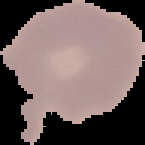

image type = segmented cell region with the area outside set to black
malaria status = uninfected
preparation = thin blood smear
image size = 145×145 pixels